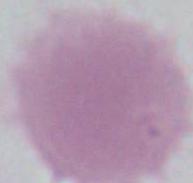
modality: photomicrograph
magnification: 1000x
identification: erythrocyte